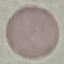

{
  "result": "no malaria parasites seen",
  "stain": "Giemsa",
  "capture": "smartphone through the microscope eyepiece",
  "image_type": "automatically extracted cell patch, resized to 64 × 64 pixels",
  "preparation": "thin blood smear"
}